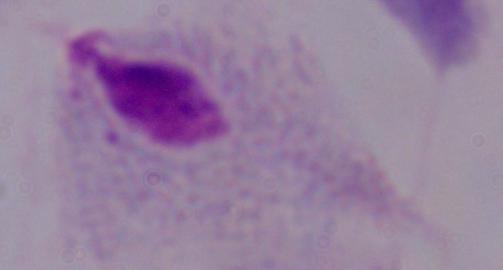
modality: photomicrograph
identification: trichomonad
magnification: 1000x